Comment on the morphology of the red blood cells.
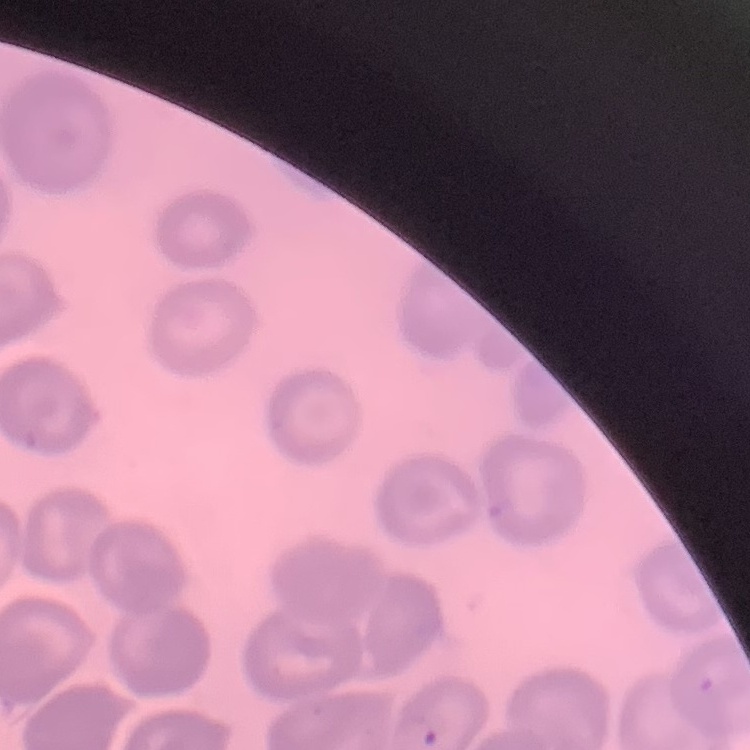
No rouleaux formation.

Stained with either Field's or Giemsa. Square crop of a larger photomicrograph. Thin blood smear.